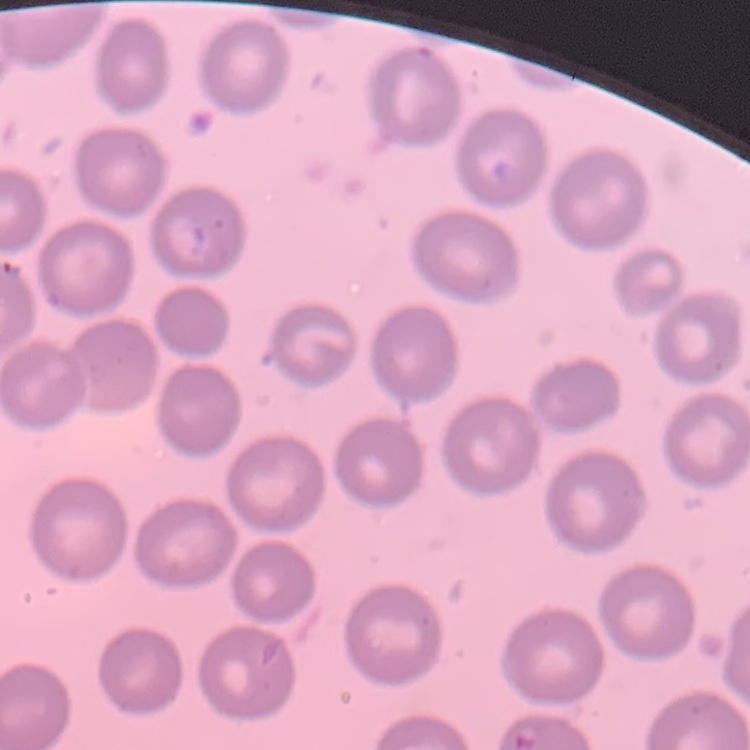 The red blood cells exhibit no rouleaux formation. Field's or Giemsa stain. Thin blood smear. Square crop of a larger photomicrograph.